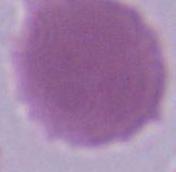
modality = photomicrograph
identification = erythrocyte
magnification = 1000x